Point out every malaria parasite.
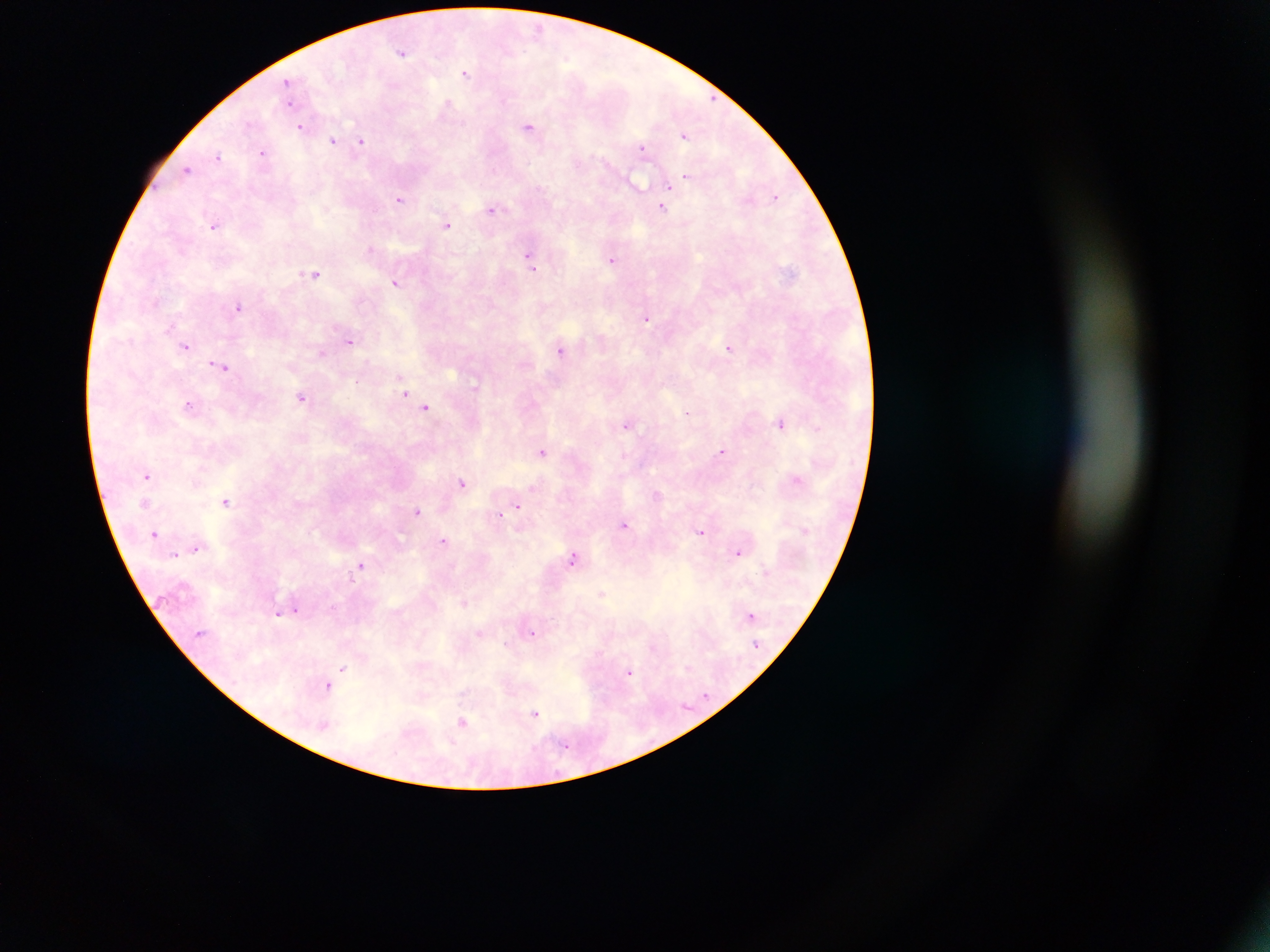

Approximate centers as {x, y} in pixels.
Malaria parasites: {537, 27}, {403, 52}, {466, 72}, {289, 83}, {447, 104}, {530, 125}, {301, 126}, {685, 134}, {334, 140}, {361, 141}, {643, 148}, {263, 153}, {218, 156}, {188, 170}, {686, 177}, {684, 180}, {670, 185}, {775, 196}, {401, 198}, {663, 207}, {492, 209}, {448, 224}, {215, 225}, {371, 249}, {530, 258}, {613, 259}, {314, 273}, {396, 283}, {239, 306}, {647, 318}, {350, 341}, {186, 346}, {729, 347}, {562, 349}, {322, 352}, {219, 365}, {406, 392}, {303, 397}, {190, 404}, {426, 408}, {687, 413}, {781, 422}, {627, 424}, {817, 428}, {543, 451}, {722, 451}, {148, 475}, {797, 479}, {462, 482}, {656, 494}, {226, 500}, {517, 505}, {418, 511}, {500, 514}, {625, 525}, {701, 531}, {157, 534}, {444, 541}, {195, 548}, {738, 552}, {574, 558}, {361, 565}, {602, 594}, {465, 602}, {288, 610}, {297, 610}, {279, 613}, {751, 615}, {481, 633}, {532, 633}, {506, 644}, {343, 668}, {629, 672}, {329, 686}, {536, 713}, {464, 721}, {566, 745}.

Single field of view. Thick blood smear. Mobile-phone photograph taken through the microscope. Image is 1270×952 pixels. Sample from Ghana.